Give the position of every malaria parasite.
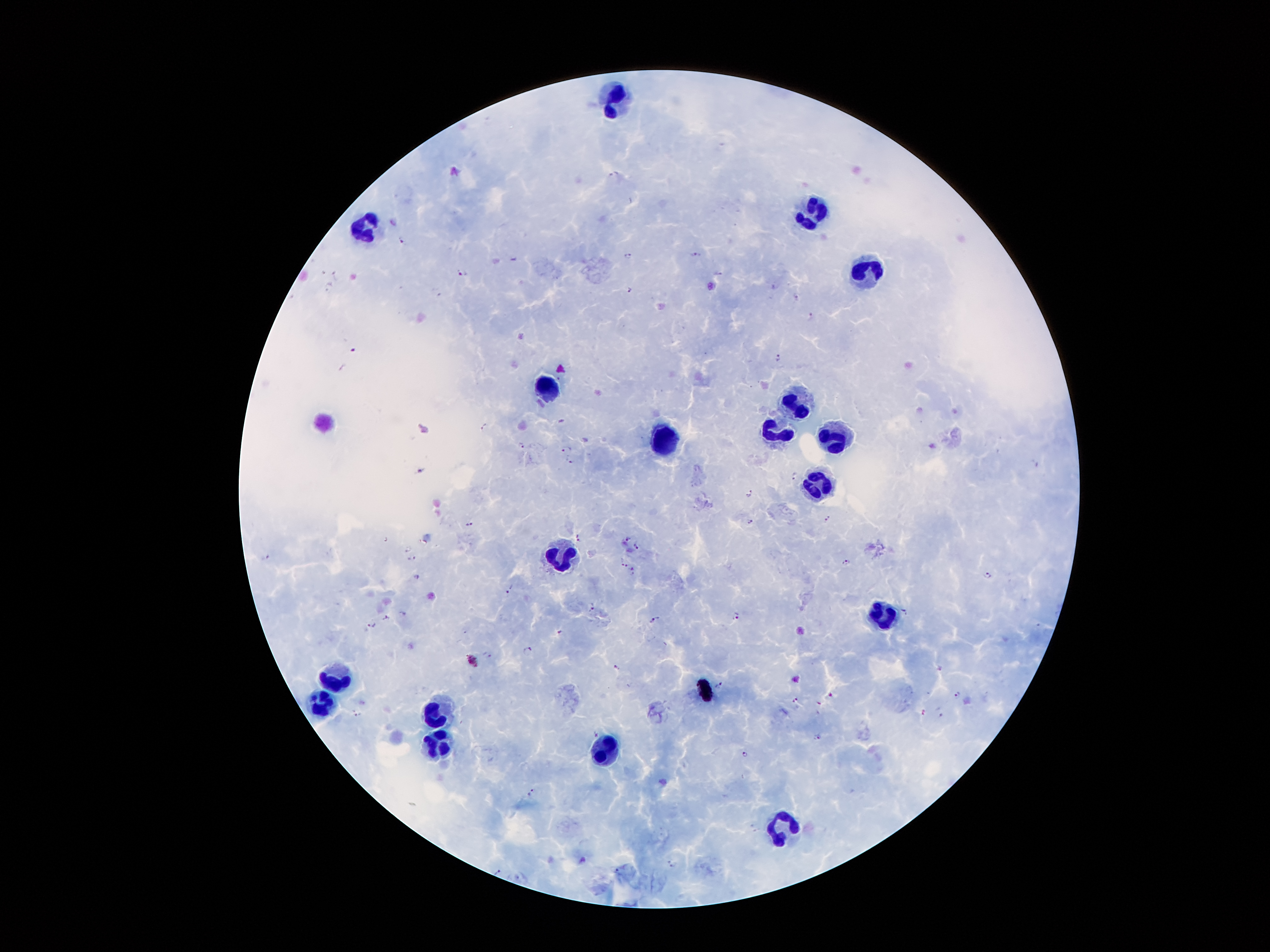
Approximate centers as {x, y} in pixels.
Malaria parasites: {614, 173}, {401, 240}, {628, 254}, {696, 255}, {463, 272}, {720, 273}, {337, 274}, {329, 284}, {630, 290}, {437, 293}, {795, 295}, {810, 312}, {351, 346}, {777, 355}, {485, 425}, {519, 443}, {564, 449}, {568, 460}, {1036, 463}, {422, 472}, {795, 475}, {749, 493}, {826, 519}, {749, 520}, {469, 524}, {579, 537}, {626, 538}, {636, 545}, {407, 549}, {267, 555}, {413, 558}, {623, 562}, {847, 563}, {633, 568}, {987, 574}, {418, 576}, {510, 588}, {593, 606}, {906, 611}, {736, 615}, {385, 617}, {655, 619}, {372, 623}, {558, 633}, {527, 647}, {488, 654}, {616, 667}, {720, 683}, {956, 694}, {796, 701}, {940, 710}, {356, 713}, {595, 733}, {815, 735}, {744, 755}, {530, 792}, {671, 864}, {497, 871}.

Leukocyte locations: {613, 98}, {814, 213}, {363, 228}, {868, 270}, {551, 389}, {793, 403}, {774, 432}, {661, 436}, {835, 438}, {819, 482}, {559, 557}, {883, 612}, {336, 678}, {324, 708}, {436, 713}, {438, 743}, {605, 752}, {781, 823}, {785, 828}. Giemsa stain. Patient malaria status: infected with Plasmodium falciparum. Thick blood film. 100x magnification. One field from this slide. Image is 1270×952 pixels. Smartphone photograph taken through the microscope eyepiece.